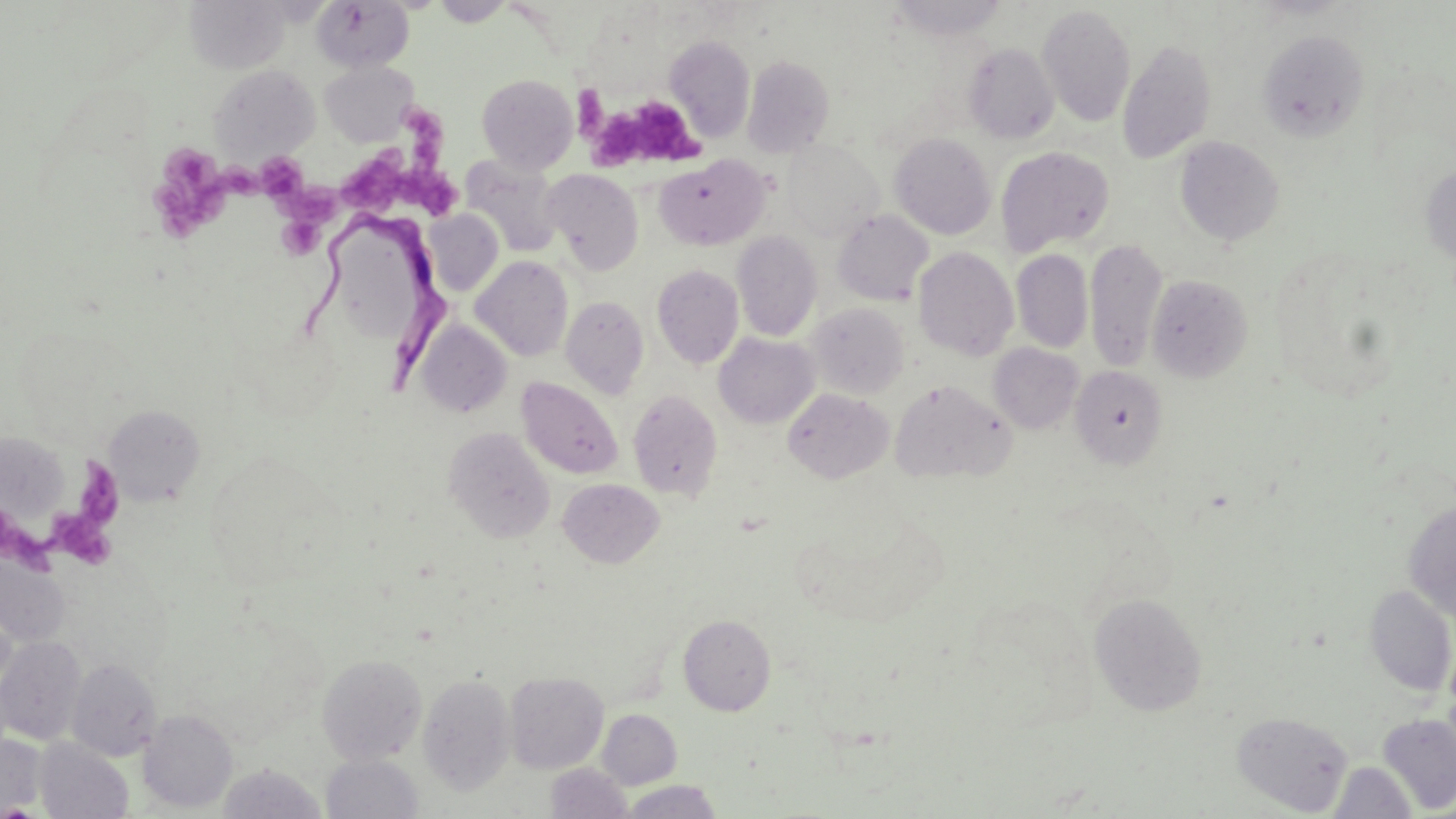
{
  "slide_level_diagnosis": "Trypanosoma brucei",
  "magnification": "1000x",
  "platelet_locations": "approximate bounding boxes as [x1, y1, x2, y2] in pixels: [572, 84, 608, 137], [594, 93, 703, 170], [334, 104, 467, 218], [151, 141, 236, 235], [233, 157, 332, 216], [278, 217, 322, 258], [76, 458, 126, 532], [52, 511, 117, 568], [3, 518, 68, 572]",
  "trypanosoma_brucei_locations": "approximate bounding boxes as [x1, y1, x2, y2] in pixels: [304, 215, 452, 389]",
  "modality": "optical microscopy",
  "uninfected_red_blood_cell_locations": "approximate bounding boxes as [x1, y1, x2, y2] in pixels: [185, 0, 290, 73], [312, 0, 414, 71], [890, 0, 1006, 40], [1038, 5, 1136, 127], [1257, 29, 1369, 142], [665, 36, 754, 141], [1117, 39, 1217, 164], [964, 43, 1059, 143], [741, 55, 835, 158], [321, 61, 419, 145], [210, 65, 320, 161], [477, 73, 578, 173], [890, 133, 996, 239], [1175, 137, 1284, 246], [783, 140, 883, 239], [996, 145, 1115, 256], [459, 154, 563, 257], [654, 155, 770, 250], [1420, 162, 1456, 269], [542, 168, 644, 274], [832, 210, 933, 306], [425, 212, 503, 295], [732, 232, 821, 341], [1085, 237, 1167, 373], [913, 247, 1018, 361], [1012, 249, 1093, 353], [471, 256, 573, 361], [652, 264, 744, 369], [1146, 273, 1251, 383], [561, 295, 649, 398], [807, 304, 910, 399], [417, 320, 512, 417], [714, 333, 819, 428], [988, 343, 1083, 433], [1070, 366, 1167, 468], [516, 376, 623, 479], [889, 378, 1014, 482], [783, 388, 894, 483], [627, 389, 723, 501], [103, 404, 205, 505], [444, 428, 554, 542], [0, 432, 68, 523], [558, 478, 664, 568], [1403, 502, 1456, 622], [0, 554, 71, 646], [1364, 584, 1455, 696], [1090, 591, 1207, 716], [678, 615, 776, 715], [0, 637, 86, 746], [317, 653, 427, 765], [66, 657, 161, 761], [505, 672, 608, 773], [418, 673, 516, 794], [138, 709, 238, 813], [598, 709, 682, 789], [1232, 710, 1353, 815], [1377, 713, 1456, 814], [0, 734, 47, 815], [34, 738, 133, 819], [321, 754, 423, 818], [1328, 760, 1417, 818], [217, 763, 327, 818], [546, 763, 633, 818], [619, 780, 725, 819]",
  "image_size": "1456×819 pixels",
  "field_of_view": "single",
  "preparation": "thin blood film",
  "stain": "May-Grünwald-Giemsa"
}